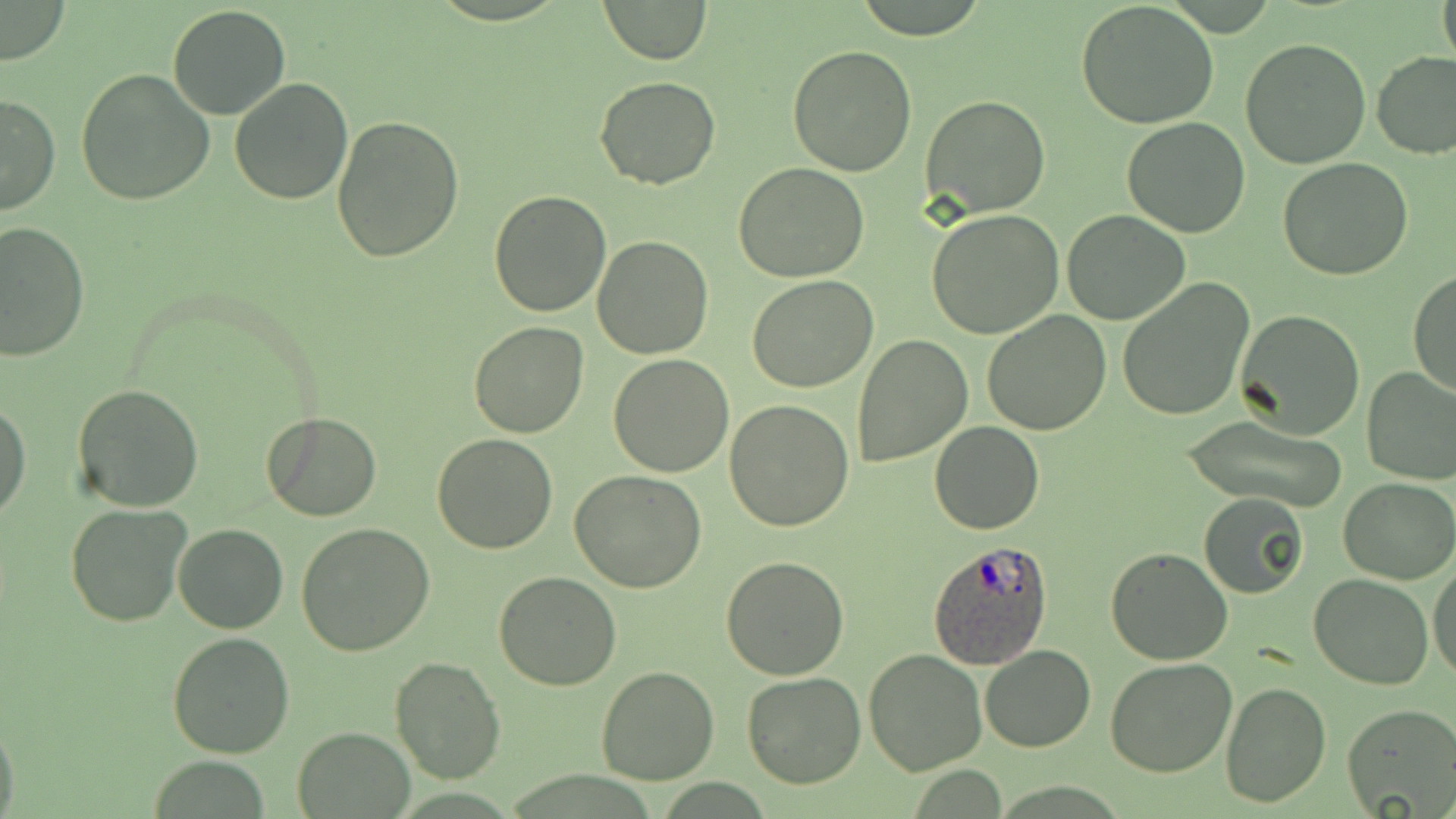
Approximate bounding boxes as (x1,y1)-(x2,y2) corner pairs in pixels. Plasmodium ovale-infected red blood cell locations: (928,541)-(1052,669). Uninfected red blood cell locations: (598,0)-(711,64), (1437,0)-(1456,69), (1075,1)-(1218,128), (0,2)-(70,65), (168,4)-(291,119), (1240,38)-(1371,170), (787,45)-(916,175), (1372,52)-(1456,159), (76,69)-(216,206), (593,75)-(721,190), (228,77)-(354,205), (0,92)-(60,214), (921,94)-(1051,218), (330,115)-(463,262), (1122,116)-(1253,238), (1278,159)-(1412,281), (733,163)-(869,282), (489,190)-(613,317), (926,208)-(1063,337), (1062,210)-(1190,326), (1,221)-(90,362), (590,236)-(713,359), (1407,268)-(1456,398), (748,274)-(878,392), (1116,279)-(1255,422), (1234,309)-(1366,439), (981,310)-(1112,435), (469,322)-(591,439), (851,334)-(973,468), (608,354)-(733,477), (1360,365)-(1456,486), (72,384)-(204,514), (0,399)-(30,522), (725,401)-(855,533), (261,413)-(383,521), (1181,414)-(1351,514), (930,420)-(1045,534), (432,433)-(560,554), (569,470)-(707,593), (1338,477)-(1455,585), (1198,491)-(1309,598), (66,503)-(192,628), (296,522)-(435,657), (173,524)-(288,633), (1105,547)-(1233,665), (721,556)-(851,679), (1429,557)-(1456,683), (493,572)-(623,692), (1308,574)-(1434,690), (167,631)-(294,758), (979,645)-(1096,754), (862,648)-(987,775), (1105,655)-(1238,776), (389,656)-(504,787), (595,666)-(720,785), (741,673)-(868,789), (1221,680)-(1331,808), (1341,703)-(1456,818), (0,714)-(20,819), (293,728)-(413,817). Slide-level diagnosis: Plasmodium ovale. May-Grünwald-Giemsa stain. Thin blood smear. One field of a larger specimen. Captured at 1000x magnification. Image is 1456×819 pixels. Light microscopy.